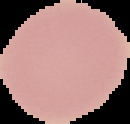
Summary:
  - Result: negative for Plasmodium parasites
  - Preparation: thin blood film
  - Image type: segmented cell region with the area outside set to black
  - Image size: 130×124 pixels